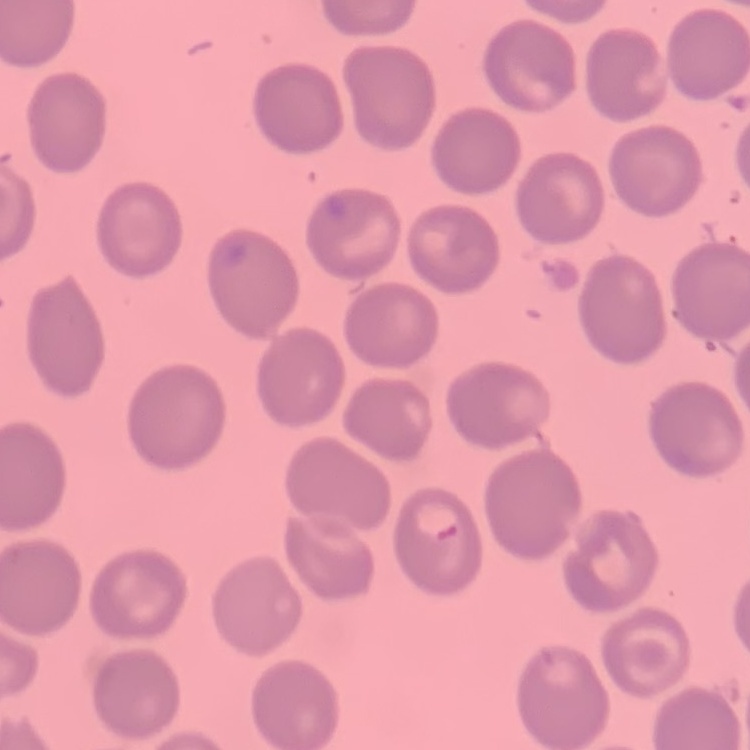

erythrocyte morphology = no rouleaux formation
image type = one tile cut from a larger photomicrograph
stain = Field's or Giemsa
preparation = thin peripheral smear